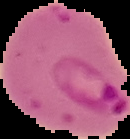

Summary:
  - Image size: 130×139 pixels
  - Preparation: thin blood smear
  - Image type: segmented cell region on a black background
  - Malaria status: parasitized